State which parasite is depicted.
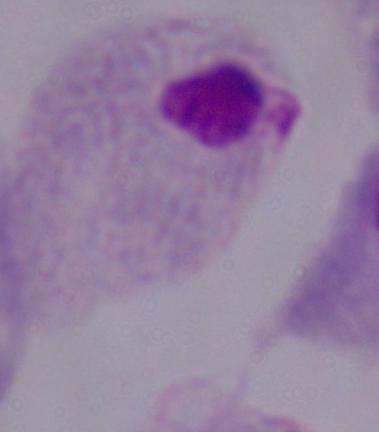

This is a trichomonad.

magnification = 1000x
modality = photomicrograph